Give the position of every leukocyte visible.
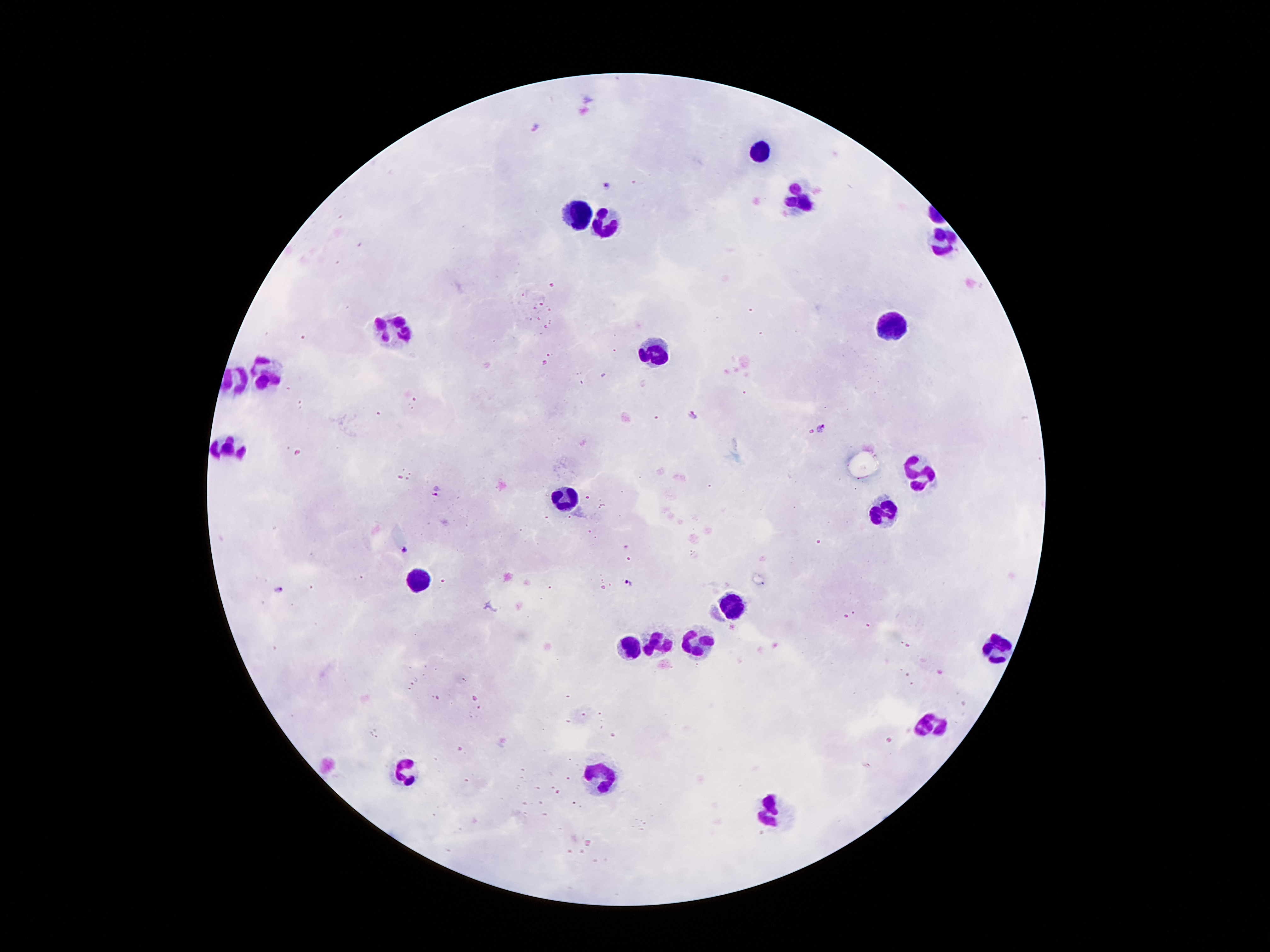

Approximate centers as {x, y} in pixels.
Leukocytes: {758, 150}, {800, 199}, {583, 213}, {608, 222}, {939, 241}, {888, 327}, {403, 329}, {659, 355}, {270, 374}, {232, 444}, {919, 472}, {566, 493}, {884, 511}, {421, 575}, {739, 602}, {659, 642}, {697, 642}, {629, 645}, {998, 651}, {930, 728}, {405, 768}, {604, 778}, {774, 813}.

Summary:
  - Malaria parasite locations: {538, 128}, {607, 185}, {696, 415}, {823, 427}, {435, 490}, {405, 551}, {628, 582}, {279, 590}
  - Capture: smartphone through the microscope eyepiece
  - Patient malaria status: positive for Plasmodium falciparum
  - Magnification: 100x
  - Field of view: single
  - Stain: Giemsa
  - Image size: 1270×952 pixels
  - Preparation: thick blood smear